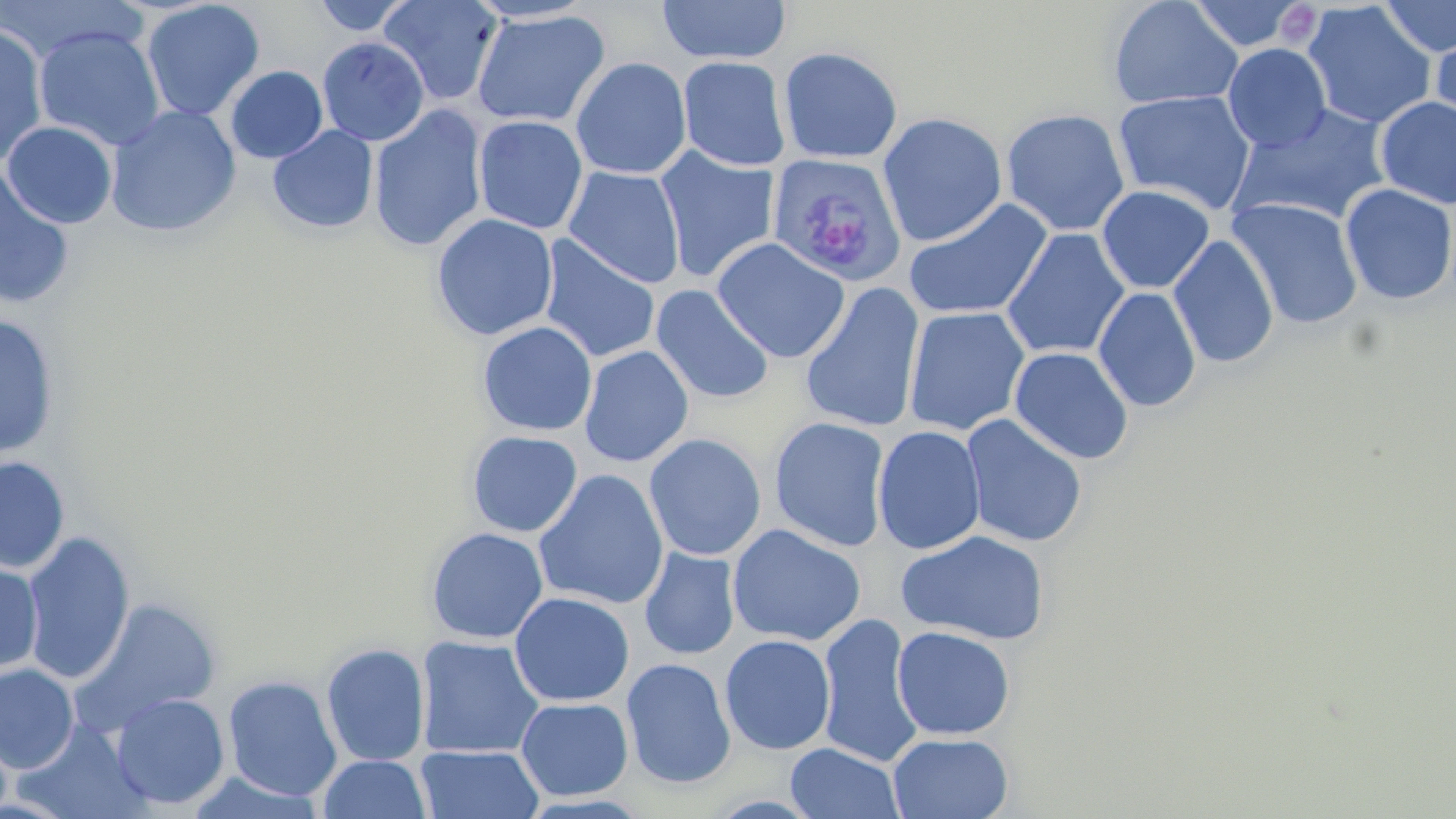

Approximate bounding boxes as [x1, y1, x2, y2] in pixels. Uninfected red blood cell locations: [311, 0, 417, 36], [378, 0, 502, 106], [466, 0, 597, 24], [657, 0, 791, 65], [1108, 0, 1243, 110], [1187, 0, 1307, 52], [1379, 0, 1456, 58], [0, 1, 146, 65], [141, 1, 265, 122], [1302, 2, 1436, 129], [471, 10, 610, 128], [1430, 21, 1455, 140], [0, 23, 49, 168], [33, 25, 166, 151], [317, 37, 429, 146], [1223, 43, 1332, 152], [778, 46, 902, 164], [677, 56, 790, 172], [570, 57, 692, 179], [225, 65, 328, 164], [1113, 90, 1256, 215], [1375, 96, 1456, 209], [369, 104, 489, 252], [1230, 104, 1393, 226], [106, 105, 242, 237], [1001, 108, 1130, 237], [877, 112, 1008, 246], [473, 115, 588, 234], [2, 120, 118, 229], [267, 125, 379, 235], [654, 147, 779, 283], [563, 166, 685, 288], [0, 167, 75, 311], [1340, 183, 1456, 306], [1096, 185, 1215, 294], [903, 198, 1053, 321], [1227, 198, 1364, 330], [431, 213, 558, 341], [1001, 228, 1130, 360], [1168, 234, 1279, 369], [537, 236, 661, 364], [712, 238, 849, 363], [800, 283, 925, 433], [650, 284, 775, 405], [1093, 287, 1202, 411], [904, 306, 1030, 437], [0, 315, 60, 459], [477, 321, 598, 437], [578, 345, 694, 467], [1010, 346, 1134, 465], [960, 413, 1088, 548], [769, 417, 891, 552], [872, 425, 986, 555], [466, 430, 583, 537], [644, 433, 766, 561], [0, 456, 70, 573], [533, 469, 669, 610], [727, 523, 866, 647], [426, 527, 548, 644], [896, 529, 1051, 646], [21, 532, 135, 684], [639, 547, 740, 660], [0, 559, 43, 678], [509, 591, 635, 706], [73, 598, 221, 732], [815, 612, 923, 767], [891, 626, 1015, 741], [719, 634, 836, 755], [416, 635, 545, 759], [321, 642, 431, 766], [621, 657, 736, 789], [0, 663, 79, 773], [222, 675, 342, 801], [111, 693, 230, 810], [516, 697, 634, 801], [888, 732, 1014, 819], [784, 742, 904, 819], [415, 745, 544, 819], [318, 754, 432, 818], [185, 771, 328, 817]. Plasmodium vivax-infected red blood cell locations: [768, 152, 908, 287]. Slide-level diagnosis: Plasmodium vivax. Thin blood smear. Captured at 1000x magnification. Light microscopy. Image is 1456×819 pixels. One field of a larger specimen. May-Grünwald-Giemsa-stained preparation.